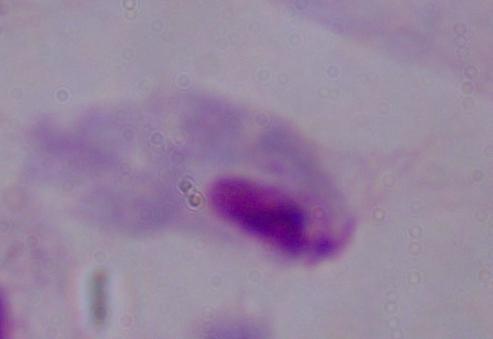
magnification = 1000x
modality = photomicrograph
identification = trichomonad